Assess this cell for malaria.
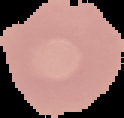
Uninfected.

Image is 124×118 pixels. From a thin blood smear. Segmented cell region on a black background.